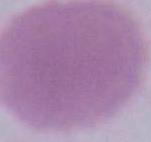

Summary:
  - Magnification: 1000x
  - Identification: red blood cell
  - Modality: micrograph